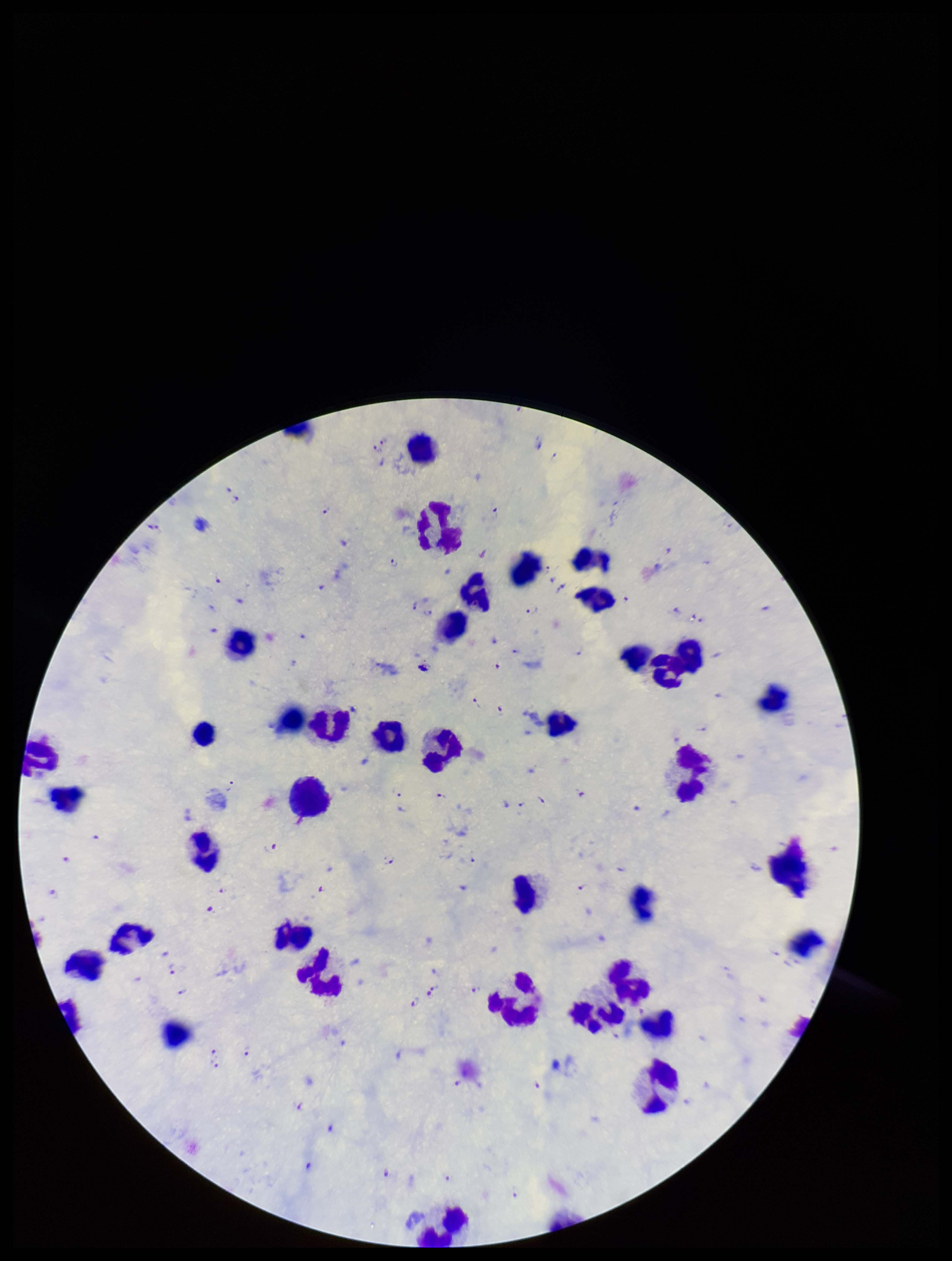

{
  "leukocyte_count": 44,
  "species_reported_for_this_patient": "Plasmodium falciparum",
  "plasmodium_parasites": "identified",
  "patient_malaria_status": "positive",
  "preparation": "thick",
  "parasite_count": 92,
  "field_of_view": "single",
  "capture": "smartphone photograph through the microscope eyepiece",
  "stain": "Giemsa",
  "image_size": "952×1261 pixels"
}